Classify this cell by malaria status.
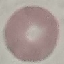
It is uninfected.

capture: smartphone camera at the microscope eyepiece
image_type: automatically extracted cell patch, resized to 64 × 64 pixels
preparation: thin blood film
stain: Giemsa